Give the position of every Plasmodium parasite visible.
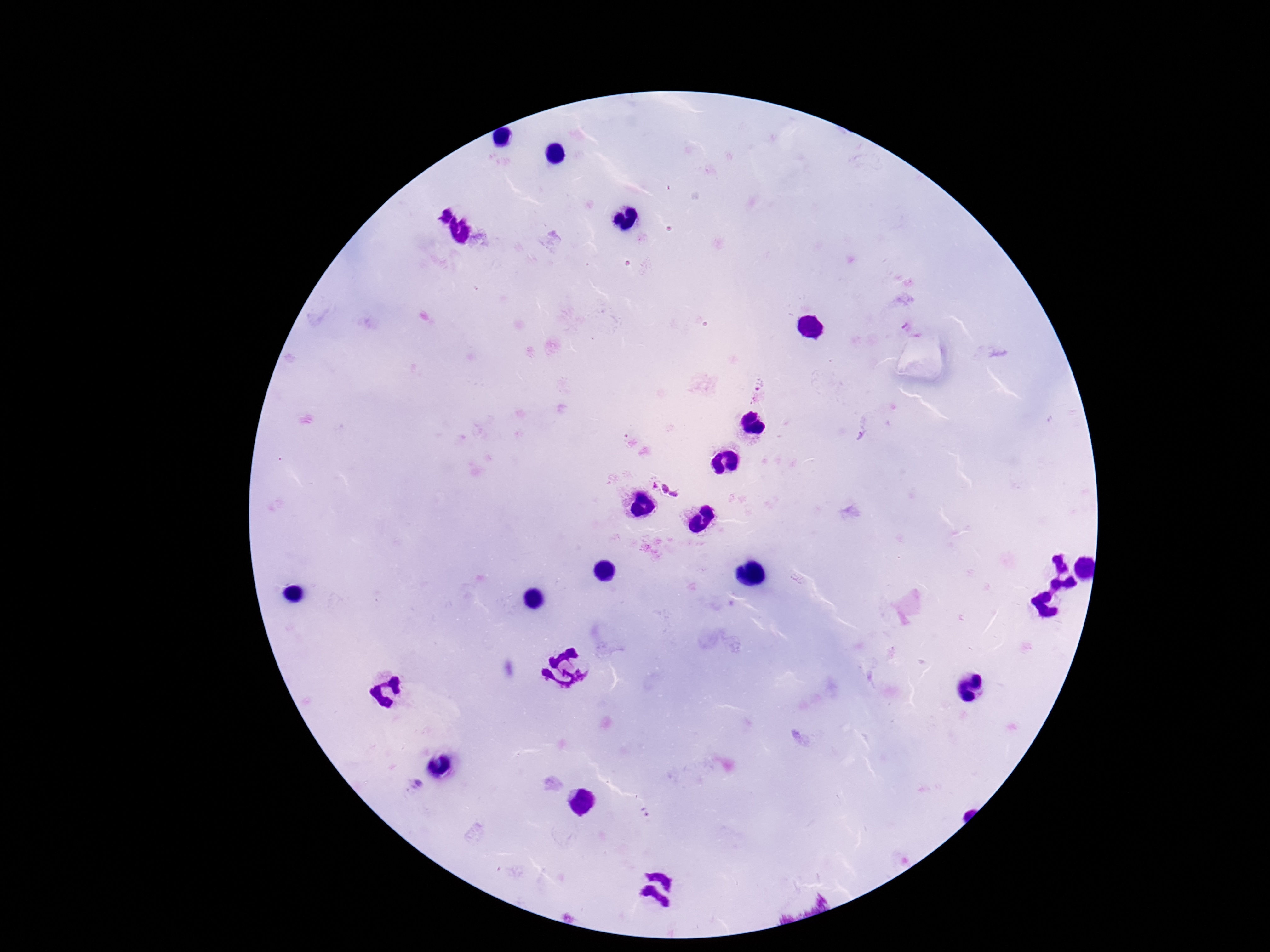
Approximate object centers, in pixels from the top-left corner.
Plasmodium parasites: (x=756, y=392), (x=666, y=486).

image_size: 1270×952 pixels
magnification: 100x
capture: smartphone camera through the microscope eyepiece
patient_malaria_status: positive
field_of_view: one from this slide
preparation: thick blood smear
stain: Giemsa